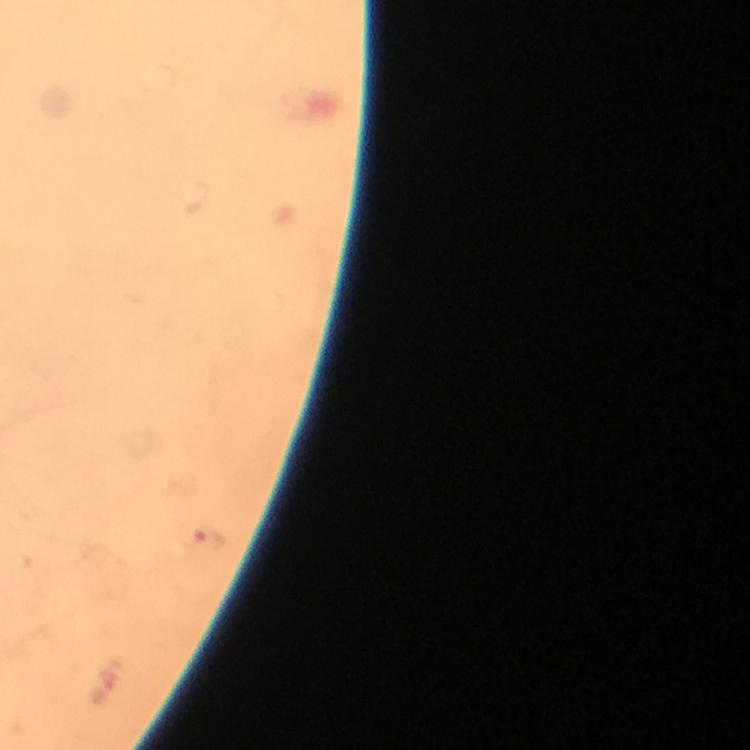
magnification = 100x
image size = 750×750 pixels
stain = Giemsa
preparation = thick blood smear
cropped from = one field of view
capture = smartphone mounted on the microscope
immersion oil = applied
malaria parasite locations = approximate object centers, in pixels from the top-left corner: (x=210, y=539)
context = from a malaria diagnostic workup